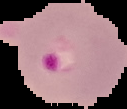

Summary:
  - Result: malaria parasites detected
  - Preparation: thin blood film
  - Image size: 127×109 pixels
  - Image type: segmented cell region with the area outside set to black